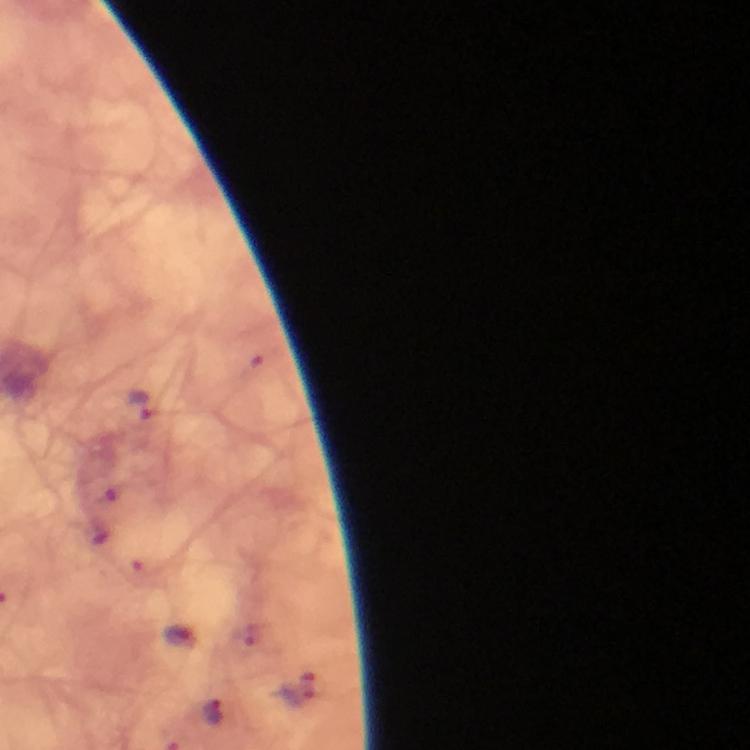
image size = 750×750 pixels
stain = Giemsa
magnification = 100x
Plasmodium parasite locations = approximate centers as (x, y) in pixels: (139, 404), (180, 635), (214, 710)
capture = smartphone camera through the microscope
cropped from = one field of view
context = from a malaria diagnostic workup
immersion oil = used
preparation = thick blood film